Report the malaria status of this cell.
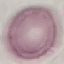

It is uninfected.

{
  "capture": "smartphone camera at the microscope eyepiece",
  "preparation": "thin blood smear",
  "stain": "Giemsa",
  "image_type": "cell patch, automatically extracted from a larger field of view and resized to 64 × 64 pixels"
}